State the blood parasite species.
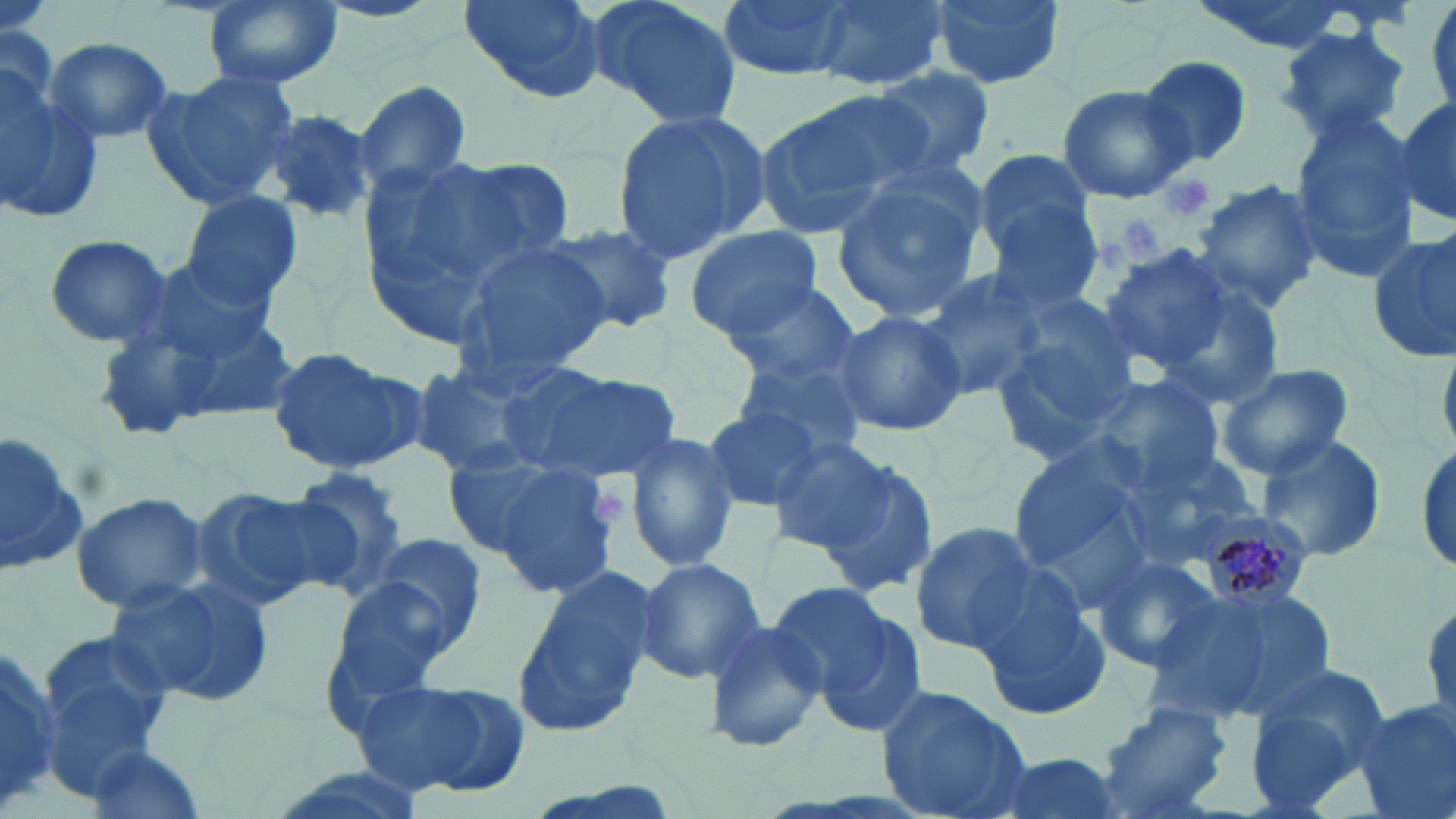
Plasmodium malariae.

{
  "field_of_view": "one of a larger specimen",
  "plasmodium_malariae_infected_red_blood_cell_locations": "approximate bounding boxes as [x1, y1, x2, y2] in pixels: [1200, 510, 1313, 613]",
  "preparation": "thin blood film",
  "image_size": "1456×819 pixels",
  "magnification": "1000x",
  "platelet_locations": "approximate bounding boxes as [x1, y1, x2, y2] in pixels: [1156, 172, 1215, 222], [1120, 217, 1165, 262], [590, 490, 626, 525]",
  "uninfected_red_blood_cell_locations": "approximate bounding boxes as [x1, y1, x2, y2] in pixels: [457, 0, 605, 103], [584, 0, 744, 134], [716, 0, 852, 77], [807, 0, 953, 91], [924, 0, 1067, 92], [1428, 0, 1456, 111], [203, 1, 339, 91], [1274, 23, 1414, 145], [42, 37, 174, 145], [1136, 55, 1254, 168], [865, 68, 993, 178], [141, 71, 299, 213], [0, 75, 104, 225], [354, 79, 474, 192], [1058, 85, 1194, 203], [755, 89, 932, 235], [1394, 98, 1456, 229], [1286, 106, 1421, 281], [258, 109, 377, 226], [611, 110, 773, 261], [972, 148, 1097, 269], [420, 152, 577, 278], [829, 168, 987, 323], [1192, 180, 1324, 312], [178, 191, 303, 311], [988, 210, 1104, 319], [540, 218, 680, 331], [684, 226, 823, 339], [1367, 226, 1455, 363], [44, 234, 172, 349], [449, 237, 611, 387], [1097, 246, 1235, 373], [914, 266, 1046, 408], [1150, 278, 1286, 407], [103, 281, 303, 433], [723, 285, 863, 392], [833, 308, 967, 436], [989, 319, 1136, 465], [263, 345, 422, 476], [735, 348, 874, 461], [404, 360, 556, 482], [1214, 362, 1353, 480], [518, 364, 680, 483], [1087, 377, 1228, 496], [699, 403, 826, 514], [1, 430, 87, 580], [621, 430, 742, 575], [1253, 431, 1388, 564], [765, 435, 894, 551], [1004, 436, 1155, 583], [1412, 436, 1454, 578], [1120, 446, 1264, 566], [455, 447, 623, 596], [818, 455, 939, 595], [284, 466, 413, 588], [191, 486, 347, 611], [70, 493, 208, 613], [908, 521, 1043, 652], [356, 532, 492, 659], [1090, 552, 1222, 672], [633, 558, 767, 685], [515, 566, 663, 742], [109, 574, 276, 710], [976, 577, 1111, 721], [320, 578, 459, 716], [1180, 580, 1343, 718], [763, 582, 894, 700], [1419, 590, 1454, 744], [815, 608, 929, 738], [700, 618, 827, 755], [36, 633, 172, 790], [0, 636, 60, 812], [1242, 663, 1391, 812], [357, 676, 530, 798], [874, 684, 1033, 819], [1353, 699, 1456, 819], [1091, 700, 1236, 819], [82, 746, 211, 818], [975, 751, 1127, 819]",
  "modality": "light microscopy",
  "stain": "May-Grünwald-Giemsa"
}